Classify the preparation.
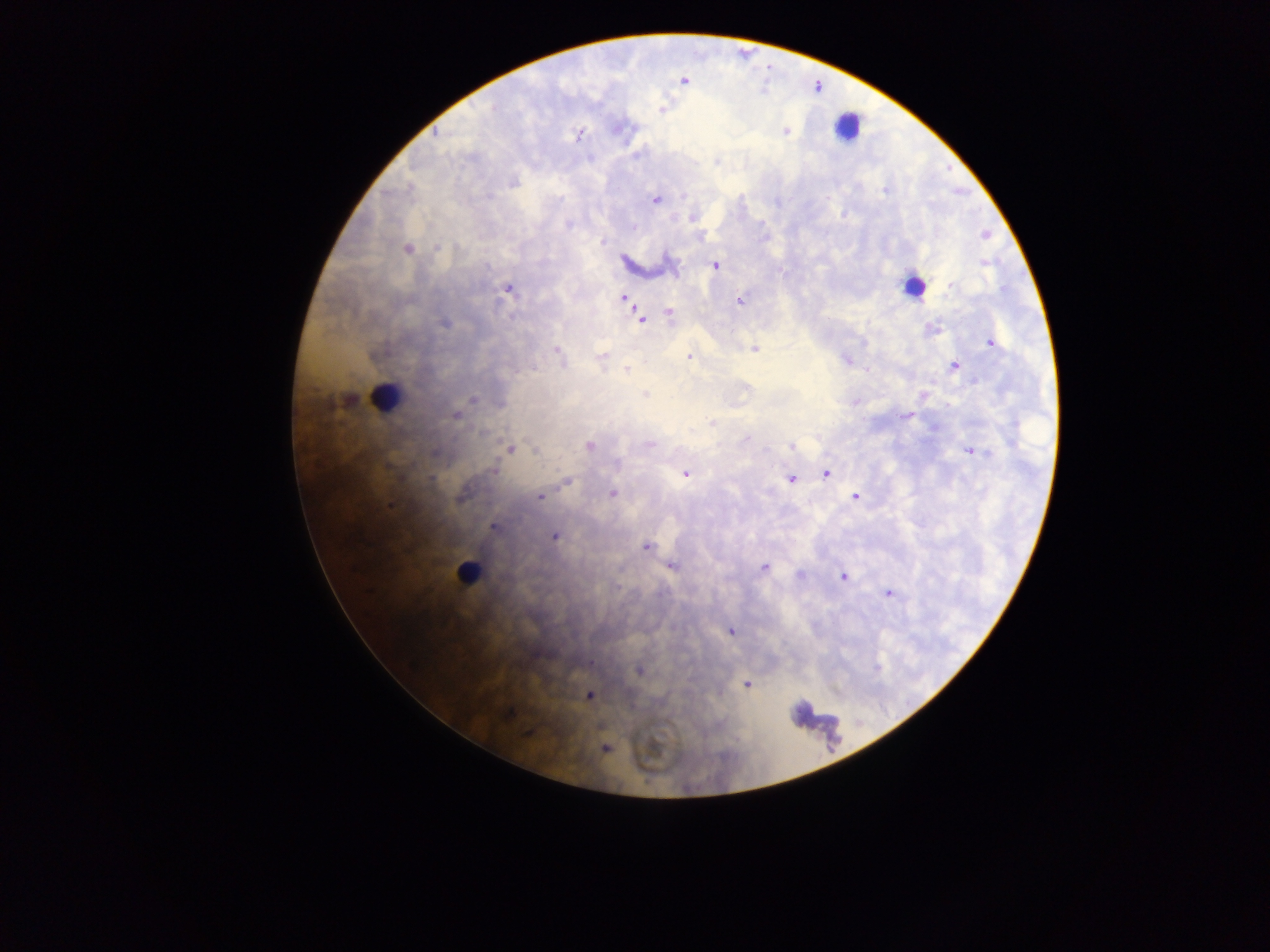

Thick blood film.

object labeled both malaria parasite and leukocyte by the source = approximate centers as (x, y) in pixels: (912, 287)
leukocyte locations = approximate centers as (x, y) in pixels: (847, 125), (386, 397), (468, 573)
capture = mobile-phone photograph through a microscope
field of view = single
country = Ghana
malaria parasite locations = approximate centers as (x, y) in pixels: (684, 81), (662, 110), (785, 131), (436, 133), (580, 133), (885, 191), (655, 199), (693, 218), (568, 225), (634, 228), (986, 235), (602, 242), (409, 250), (984, 262), (715, 265), (951, 286), (508, 288), (624, 298), (740, 301), (670, 312), (640, 318), (444, 323), (991, 343), (754, 349), (557, 350), (688, 356), (602, 357), (846, 360), (955, 367), (626, 369), (645, 396), (473, 400), (456, 415), (905, 415), (712, 423), (747, 439), (589, 445), (649, 445), (792, 447), (511, 449), (535, 450), (975, 452), (617, 465), (494, 469), (826, 473), (685, 474), (429, 479), (791, 479), (567, 481), (612, 493), (855, 496), (540, 497), (493, 527), (555, 537), (645, 547), (672, 565), (765, 568), (800, 574), (843, 576), (888, 593), (731, 631), (638, 670), (747, 685), (590, 695), (506, 715), (526, 734), (605, 749)
image size = 1270×952 pixels